Identify the preparation type.
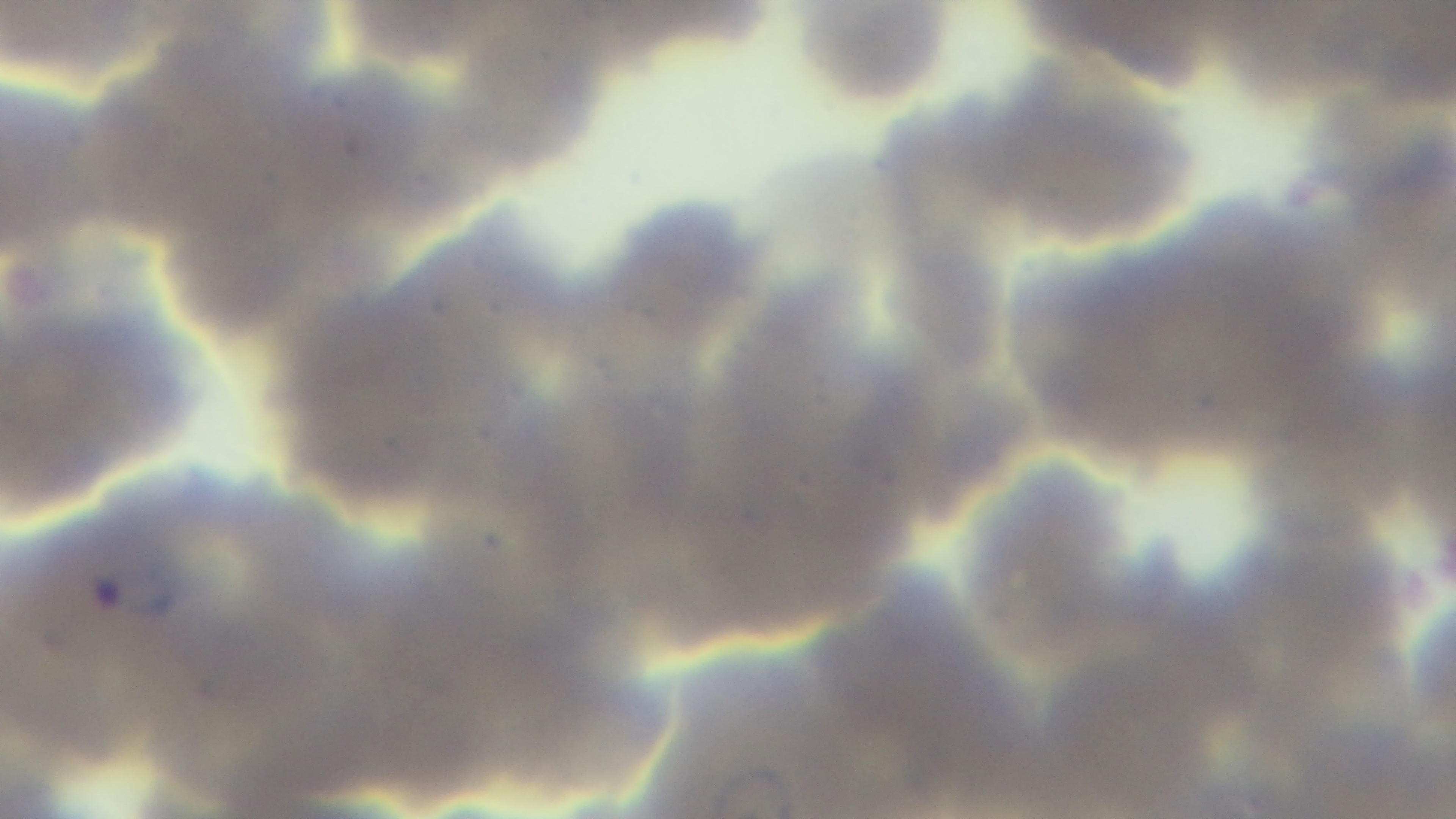

Thin.

Giemsa-stained. 100x oil-immersion objective. One field from the slide. Malaria status: positive. Mounted 4K digital camera. Photomicrograph.